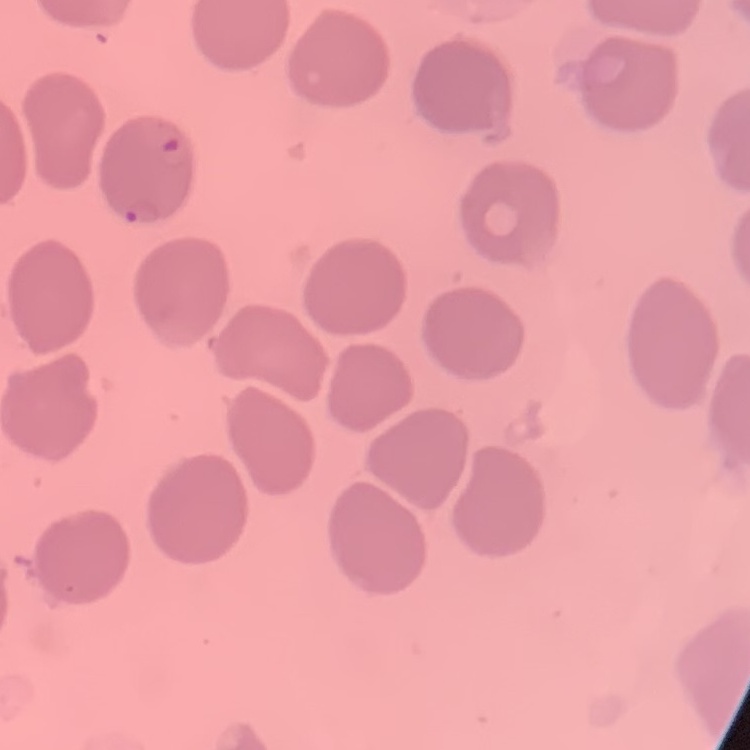

red blood cell morphology = no rouleaux formation
stain = Field's or Giemsa
image type = square crop of a larger photomicrograph
preparation = thin blood smear